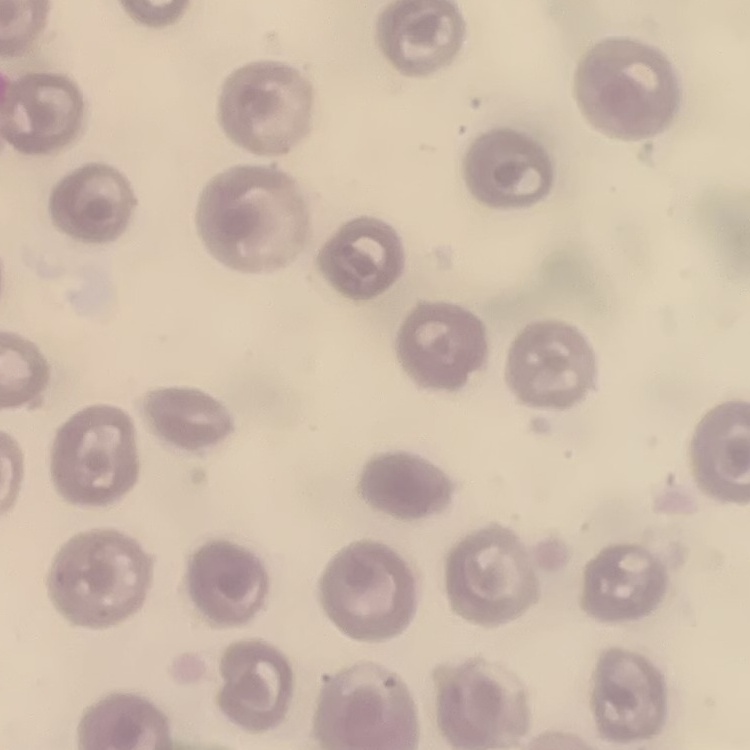 The erythrocytes show no rouleaux formation. Stained with either Field's or Giemsa. One tile cut from a larger photomicrograph. Thin blood film.